Classify this cell by malaria status.
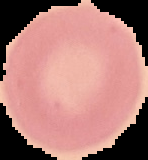
Uninfected.

{
  "image_size": "148×160 pixels",
  "preparation": "thin blood smear",
  "image_type": "segmented cell region on a black background"
}